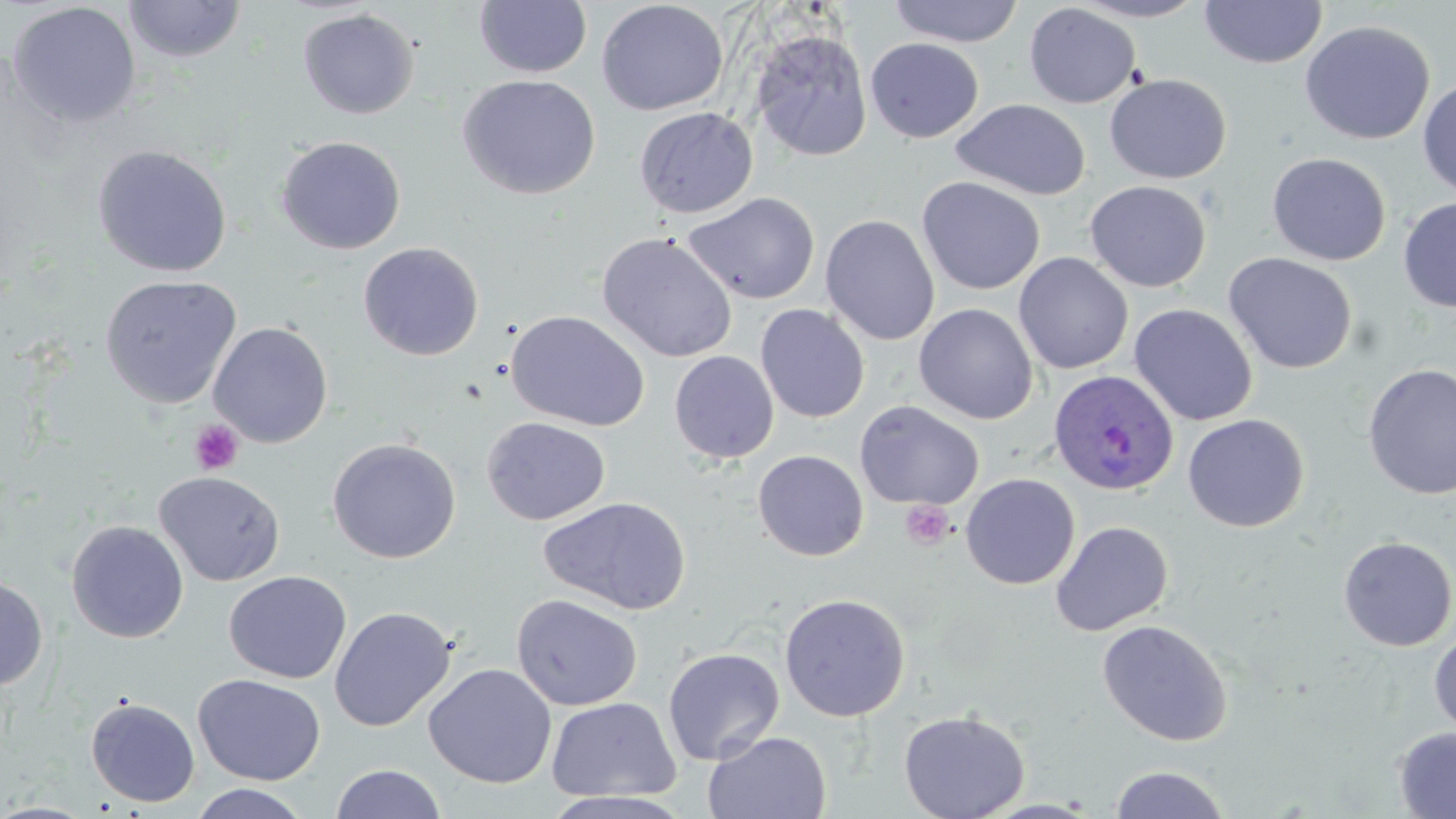 Approximate bounding boxes as (x1,y1)-(x2,y2) corner pairs in pixels. Plasmodium ovale-infected red blood cell locations: (1048,369)-(1179,498). Platelet locations: (190,419)-(244,475), (900,500)-(956,550). Uninfected red blood cell locations: (889,0)-(1024,47), (1070,0)-(1211,22), (123,1)-(247,63), (474,1)-(592,78), (596,1)-(729,116), (1198,1)-(1327,70), (6,2)-(141,128), (1024,3)-(1142,108), (297,9)-(420,119), (1299,20)-(1435,145), (749,27)-(873,162), (865,37)-(984,143), (1104,73)-(1231,184), (458,75)-(601,200), (1417,78)-(1456,199), (951,98)-(1091,200), (634,107)-(758,218), (275,135)-(406,254), (92,144)-(233,278), (1266,152)-(1391,266), (917,176)-(1045,295), (1084,180)-(1212,292), (683,192)-(820,305), (1398,196)-(1456,313), (820,214)-(940,346), (596,232)-(738,363), (358,242)-(484,360), (1013,252)-(1133,374), (1223,252)-(1358,374), (100,275)-(242,408), (755,303)-(870,423), (913,303)-(1038,425), (1128,303)-(1258,426), (506,310)-(649,431), (208,322)-(333,448), (669,350)-(780,464), (1361,363)-(1456,501), (854,400)-(984,510), (1182,413)-(1310,533), (482,417)-(610,525), (327,437)-(461,564), (752,450)-(869,561), (154,470)-(286,587), (960,472)-(1080,590), (538,496)-(692,616), (66,520)-(189,644), (1050,520)-(1173,636), (1337,536)-(1456,651), (224,570)-(352,684), (0,574)-(48,691), (779,592)-(910,722), (511,594)-(643,711), (329,606)-(455,732), (1097,619)-(1233,747), (1429,631)-(1456,739), (662,646)-(785,766), (423,663)-(557,789), (192,673)-(326,786), (546,695)-(682,804), (86,697)-(200,807), (898,709)-(1030,819), (1393,727)-(1456,819), (704,731)-(831,819), (330,764)-(447,819), (1109,765)-(1233,819), (187,783)-(314,819). Slide-level diagnosis: Plasmodium ovale. Optical microscopy. Image is 1456×819 pixels. Single field of view. Thin blood film. Captured at 1000x magnification. May-Grünwald-Giemsa stain.